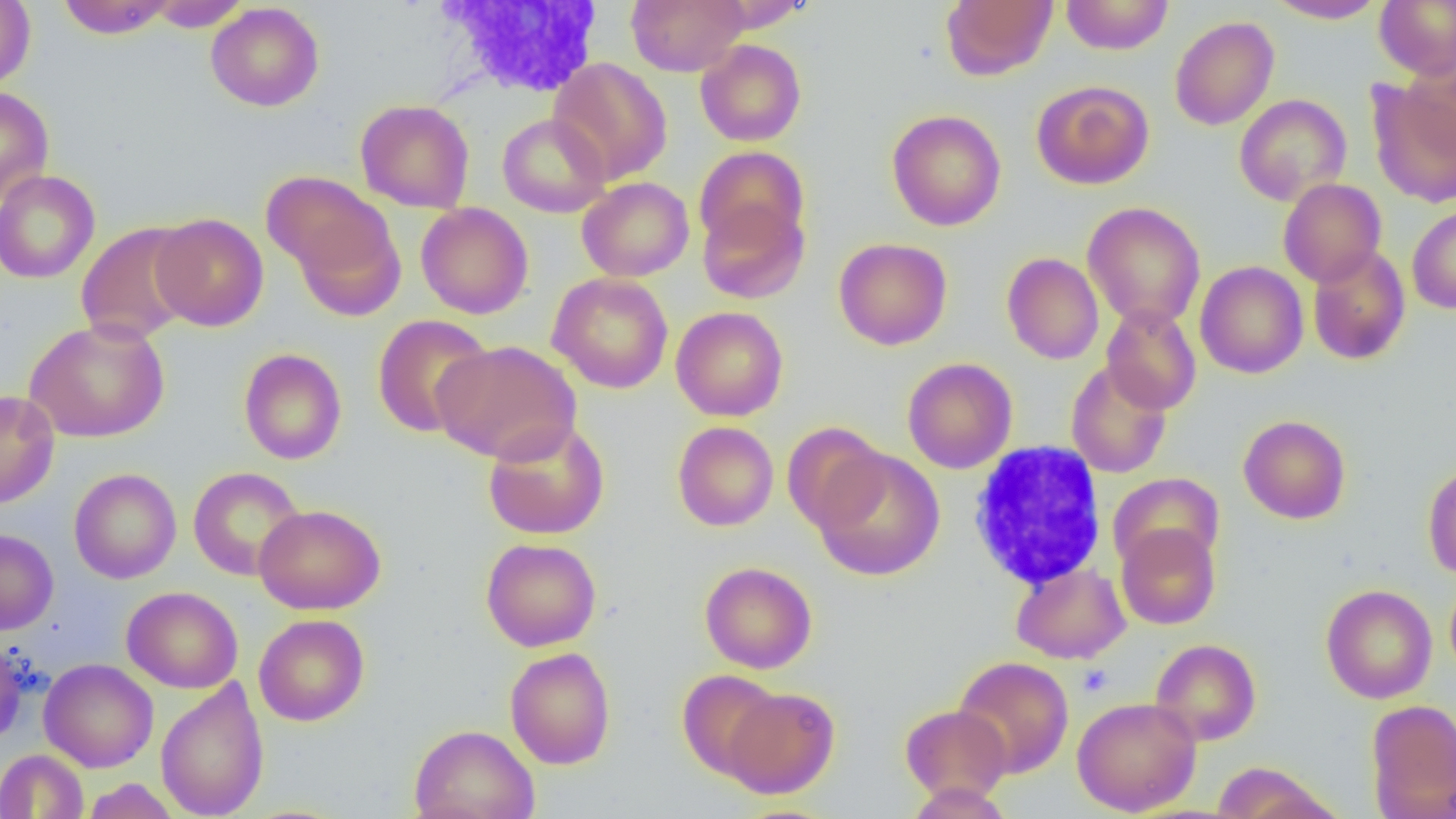

Summary:
  - Coordinate format: approximate bounding boxes as [x1, y1, x2, y2] in pixels
  - Platelet locations: [1077, 664, 1112, 697]
  - White blood cell locations: [434, 1, 609, 98], [968, 441, 1107, 591]
  - Uninfected red blood cell locations: [55, 0, 178, 39], [627, 0, 747, 76], [941, 0, 1058, 81], [941, 0, 1174, 64], [1061, 0, 1174, 55], [1267, 0, 1387, 23], [1374, 0, 1456, 79], [0, 1, 35, 91], [144, 1, 250, 31], [705, 1, 813, 32], [205, 3, 325, 112], [1169, 15, 1280, 131], [696, 39, 806, 146], [549, 57, 672, 184], [1400, 60, 1455, 163], [1367, 79, 1456, 208], [1031, 80, 1154, 190], [0, 86, 55, 207], [1234, 93, 1352, 205], [355, 99, 475, 213], [886, 110, 1006, 231], [497, 113, 611, 217], [694, 145, 809, 255], [0, 169, 101, 284], [262, 171, 397, 297], [577, 176, 694, 281], [1278, 178, 1387, 287], [697, 195, 809, 305], [1082, 202, 1206, 330], [416, 203, 534, 320], [1407, 205, 1456, 315], [151, 213, 269, 331], [75, 221, 200, 345], [833, 237, 952, 350], [1307, 245, 1411, 366], [1002, 252, 1104, 365], [1195, 261, 1308, 378], [547, 272, 673, 394], [1101, 304, 1202, 415], [671, 305, 789, 421], [371, 313, 494, 438], [24, 317, 170, 443], [430, 340, 581, 465], [239, 348, 347, 464], [902, 357, 1017, 474], [1066, 361, 1173, 478], [0, 390, 60, 509], [1238, 415, 1351, 524], [483, 419, 610, 541], [672, 421, 779, 531], [783, 421, 890, 534], [812, 448, 946, 582], [1422, 463, 1456, 580], [188, 466, 306, 581], [69, 467, 182, 584], [1108, 472, 1225, 574], [254, 503, 386, 615], [1116, 522, 1220, 630], [0, 528, 59, 634], [480, 537, 602, 651], [699, 561, 817, 674], [1011, 563, 1130, 664], [1444, 573, 1456, 683], [1321, 584, 1438, 704], [122, 585, 243, 693], [254, 613, 370, 726], [0, 637, 28, 746], [1150, 638, 1261, 745], [504, 647, 616, 770], [953, 656, 1074, 778], [39, 658, 159, 772], [677, 669, 783, 780], [155, 677, 270, 819], [722, 686, 840, 799], [1072, 696, 1201, 816], [1365, 699, 1456, 819], [900, 704, 1012, 803], [409, 724, 540, 819], [0, 749, 89, 818], [1211, 761, 1331, 819], [83, 779, 181, 818], [906, 783, 1013, 818]
  - Slide-level diagnosis: no evidence of blood parasites
  - Image size: 1456×819 pixels
  - Field of view: single
  - Magnification: 1000x
  - Preparation: thin blood smear
  - Modality: light microscopy